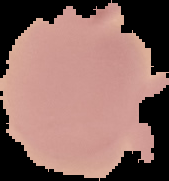

image size = 169×181 pixels
preparation = thin blood film
image type = segmented cell region with the area outside set to black
malaria status = uninfected